Classify this cell by malaria status.
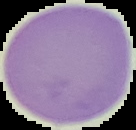

It is uninfected.

Segmented cell region on a black background. Image is 136×130 pixels. From a thin blood film.